Describe the morphology of the red blood cells.
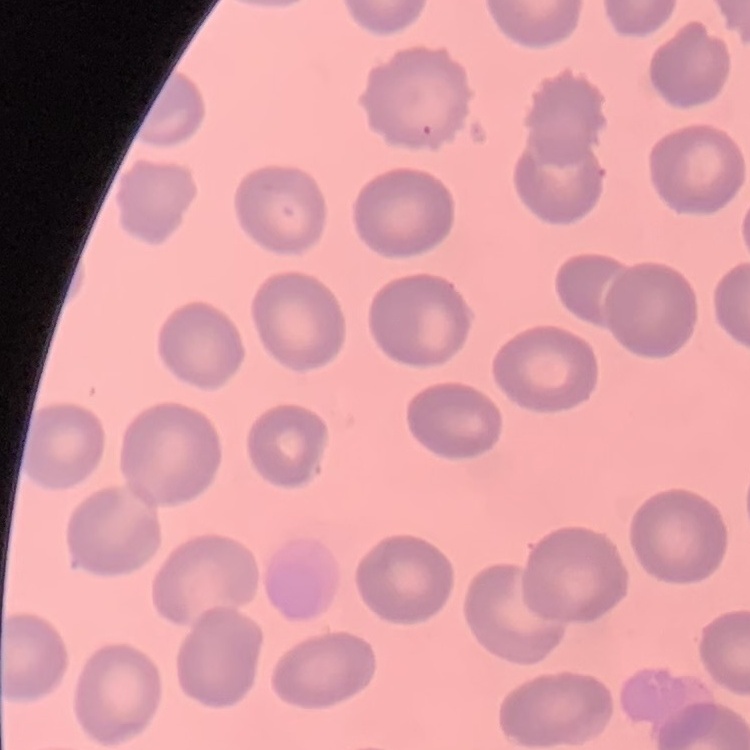

They show no rouleaux formation.

{
  "image_type": "square crop of a larger photomicrograph",
  "stain": "Field's or Giemsa",
  "preparation": "thin peripheral smear"
}